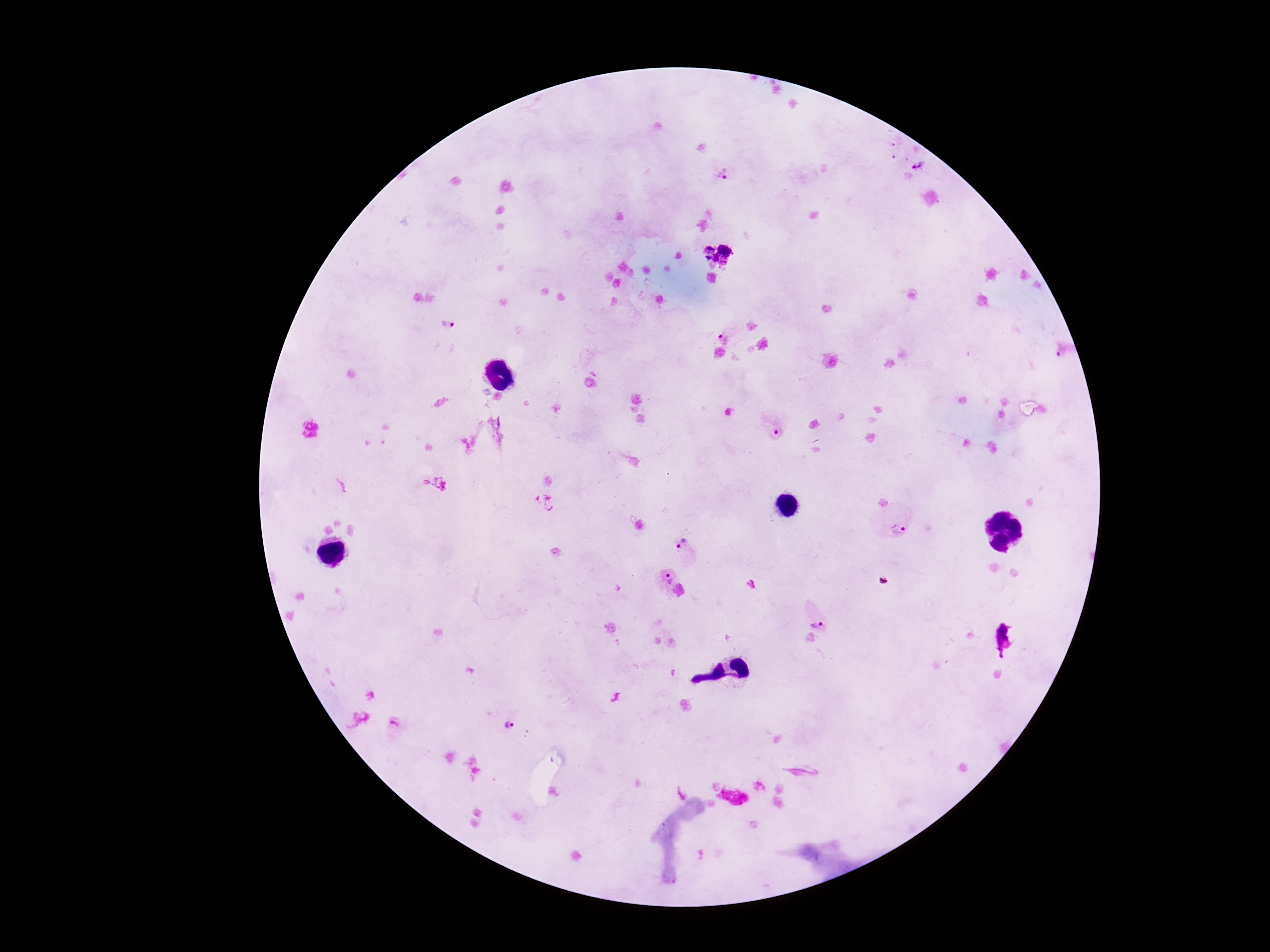

Approximate object centers, in pixels from the top-left corner.
Summary:
  - Plasmodium parasite locations: (x=912, y=160), (x=720, y=173), (x=444, y=326), (x=731, y=332), (x=436, y=483), (x=890, y=523), (x=685, y=549), (x=661, y=577), (x=816, y=615), (x=507, y=724), (x=395, y=728)
  - Image size: 1270×952 pixels
  - Field of view: one from this slide
  - Preparation: thick blood film
  - Patient malaria status: positive
  - Capture: smartphone camera through the microscope eyepiece
  - Stain: Giemsa
  - Magnification: 100x